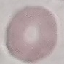 Malaria status: uninfected. Giemsa stain. Thin smear of blood. Cell patch, automatically extracted from a larger field of view and resized to 64 × 64 pixels. Photographed with a smartphone camera at the microscope eyepiece.